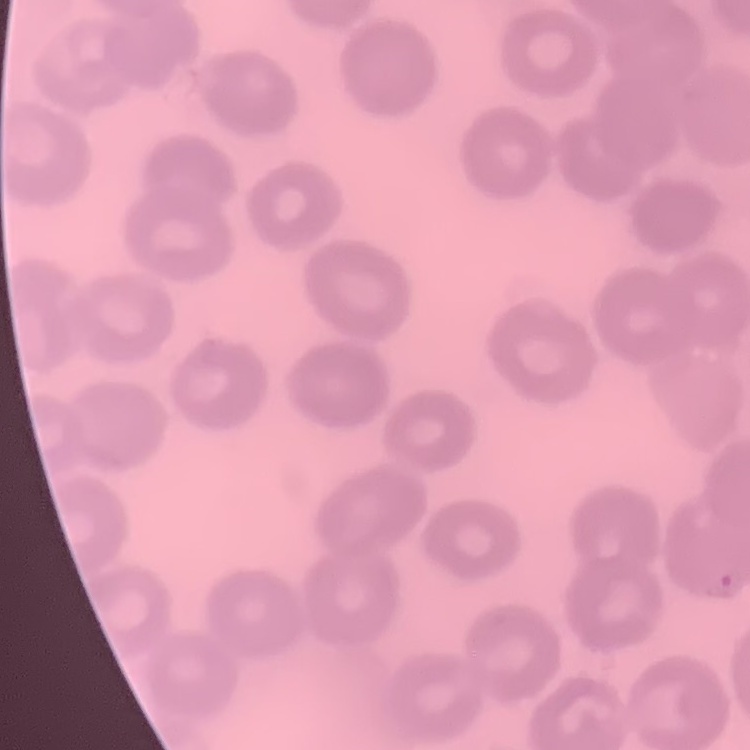 The erythrocytes exhibit no rouleaux formation. One tile cut from a larger photomicrograph. Thin blood smear. Stained with either Field's or Giemsa.